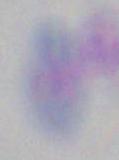

Photomicrograph. Toxoplasma gondii is shown. 1000x magnification.